Point out each malaria parasite.
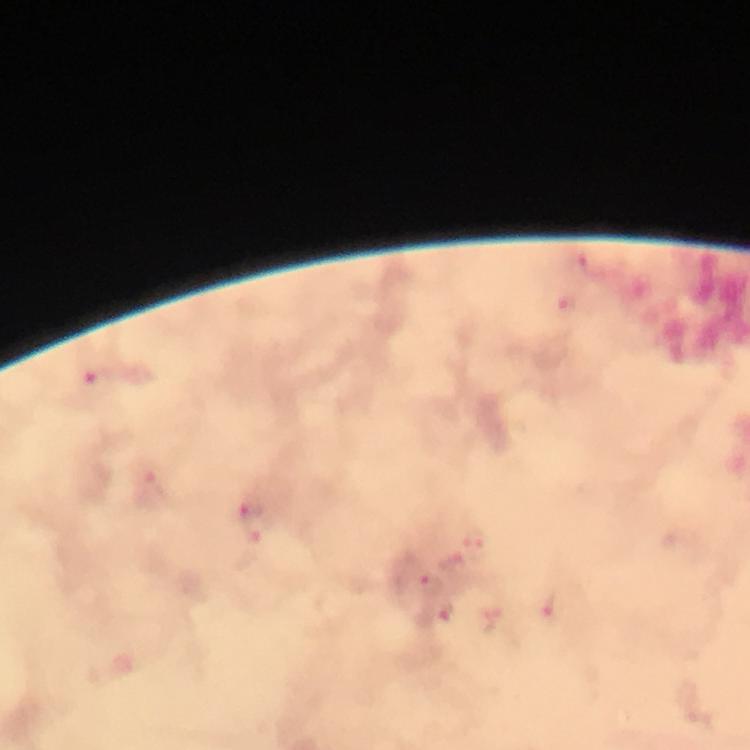
Approximate object centers, in pixels from the top-left corner.
Malaria parasites: (x=592, y=264), (x=568, y=304), (x=98, y=380), (x=252, y=510), (x=477, y=549), (x=430, y=586), (x=555, y=610), (x=442, y=613).

Thick blood film. At 100x magnification. Image is 750×750 pixels. Immersion oil was used. From a diagnostic examination for malaria. A crop from one field of view. Smartphone photograph taken through a microscope. Giemsa-stained preparation.